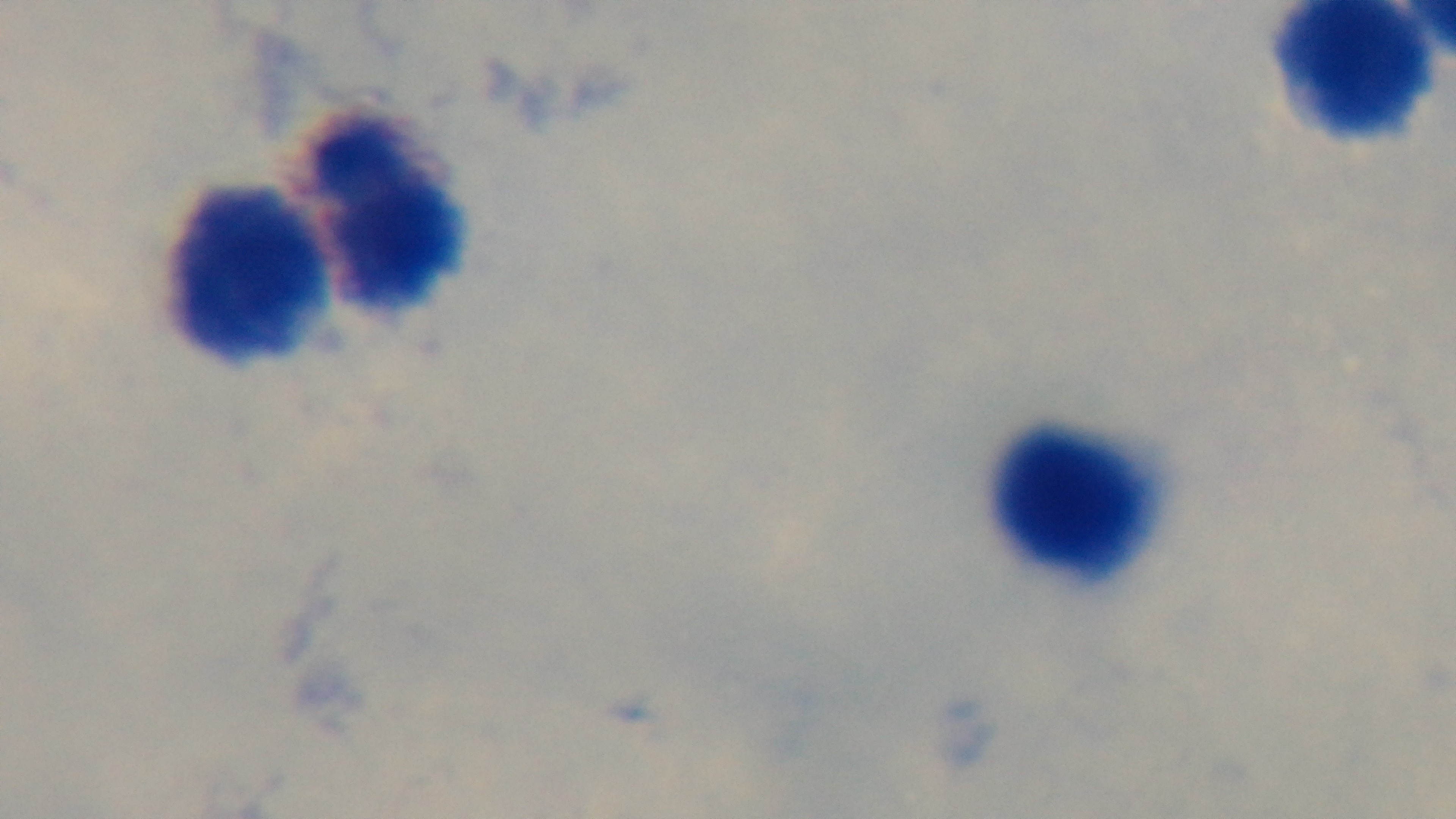
Summary:
  - Objective: 100x oil immersion
  - Modality: light microscopy
  - Preparation: thick smear
  - Field of view: one from the slide
  - Stain: Giemsa
  - Capture: mounted 4K digital camera
  - Malaria status: negative